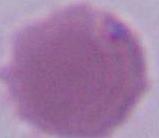

identification = red blood cell
modality = micrograph
magnification = 1000x